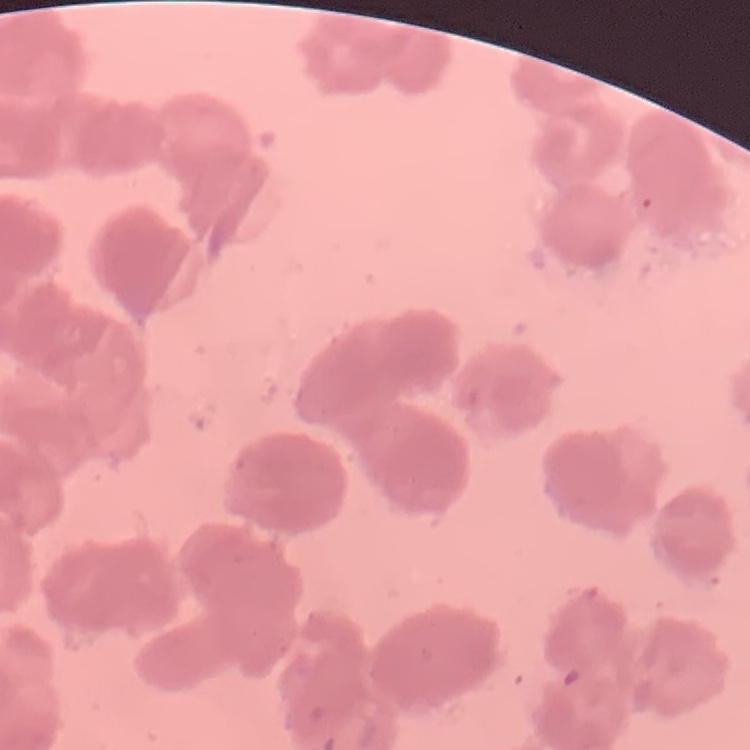
The red blood cells show rouleaux formation. Thin blood smear. One tile cut from a larger photomicrograph. Stained with either Field's or Giemsa.